State the blood parasite species.
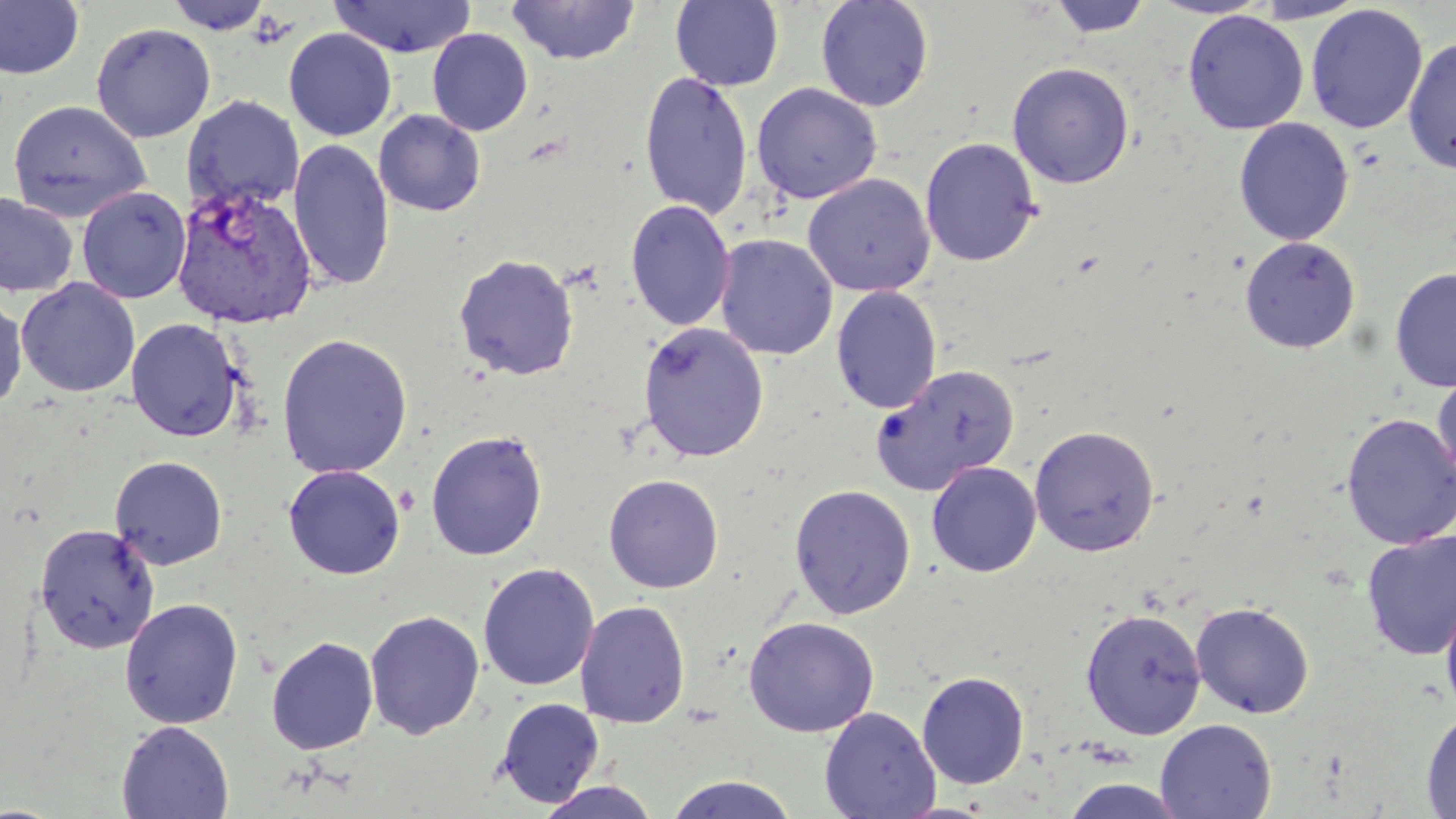

Plasmodium vivax.

preparation = thin blood smear
magnification = 1000x
modality = light microscopy
field of view = one of a larger specimen
stain = May-Grünwald-Giemsa
image size = 1456×819 pixels
Plasmodium vivax-infected red blood cell locations = approximate bounding boxes as [x1, y1, x2, y2] in pixels: [172, 184, 318, 329]
uninfected red blood cell locations = approximate bounding boxes as [x1, y1, x2, y2] in pixels: [163, 0, 276, 34], [328, 0, 477, 58], [670, 0, 784, 92], [815, 0, 935, 112], [1048, 0, 1153, 38], [1147, 0, 1275, 20], [1250, 0, 1369, 23], [0, 1, 84, 80], [505, 1, 641, 65], [1305, 4, 1429, 134], [1182, 11, 1309, 134], [91, 22, 216, 143], [283, 28, 397, 141], [426, 28, 533, 136], [1403, 35, 1456, 174], [1007, 61, 1134, 189], [639, 69, 753, 220], [751, 82, 882, 204], [182, 95, 304, 213], [6, 99, 151, 222], [374, 109, 486, 217], [1233, 118, 1354, 246], [920, 137, 1042, 267], [288, 138, 395, 291], [802, 173, 936, 296], [76, 186, 191, 304], [0, 192, 79, 298], [625, 199, 735, 332], [715, 234, 838, 360], [1239, 236, 1361, 354], [453, 253, 580, 381], [1390, 267, 1456, 393], [16, 278, 140, 397], [831, 286, 942, 415], [0, 293, 27, 414], [126, 318, 245, 442], [638, 321, 769, 462], [276, 332, 413, 478], [871, 364, 1020, 496], [1431, 371, 1456, 491], [1340, 413, 1456, 550], [1029, 424, 1161, 556], [425, 428, 548, 561], [109, 455, 228, 570], [927, 462, 1042, 577], [283, 464, 405, 579], [603, 473, 724, 593], [788, 484, 916, 619], [34, 522, 160, 654], [1361, 529, 1456, 660], [477, 563, 599, 691], [1440, 589, 1456, 721], [119, 597, 243, 729], [575, 600, 690, 728], [1190, 602, 1315, 719], [1080, 608, 1206, 738], [364, 610, 485, 740], [743, 616, 879, 737], [265, 635, 379, 755], [917, 671, 1030, 789], [494, 696, 605, 807], [819, 706, 940, 819], [1421, 708, 1456, 817], [1155, 718, 1277, 819], [117, 720, 234, 819], [662, 775, 801, 819], [1058, 779, 1189, 818], [534, 780, 662, 819]